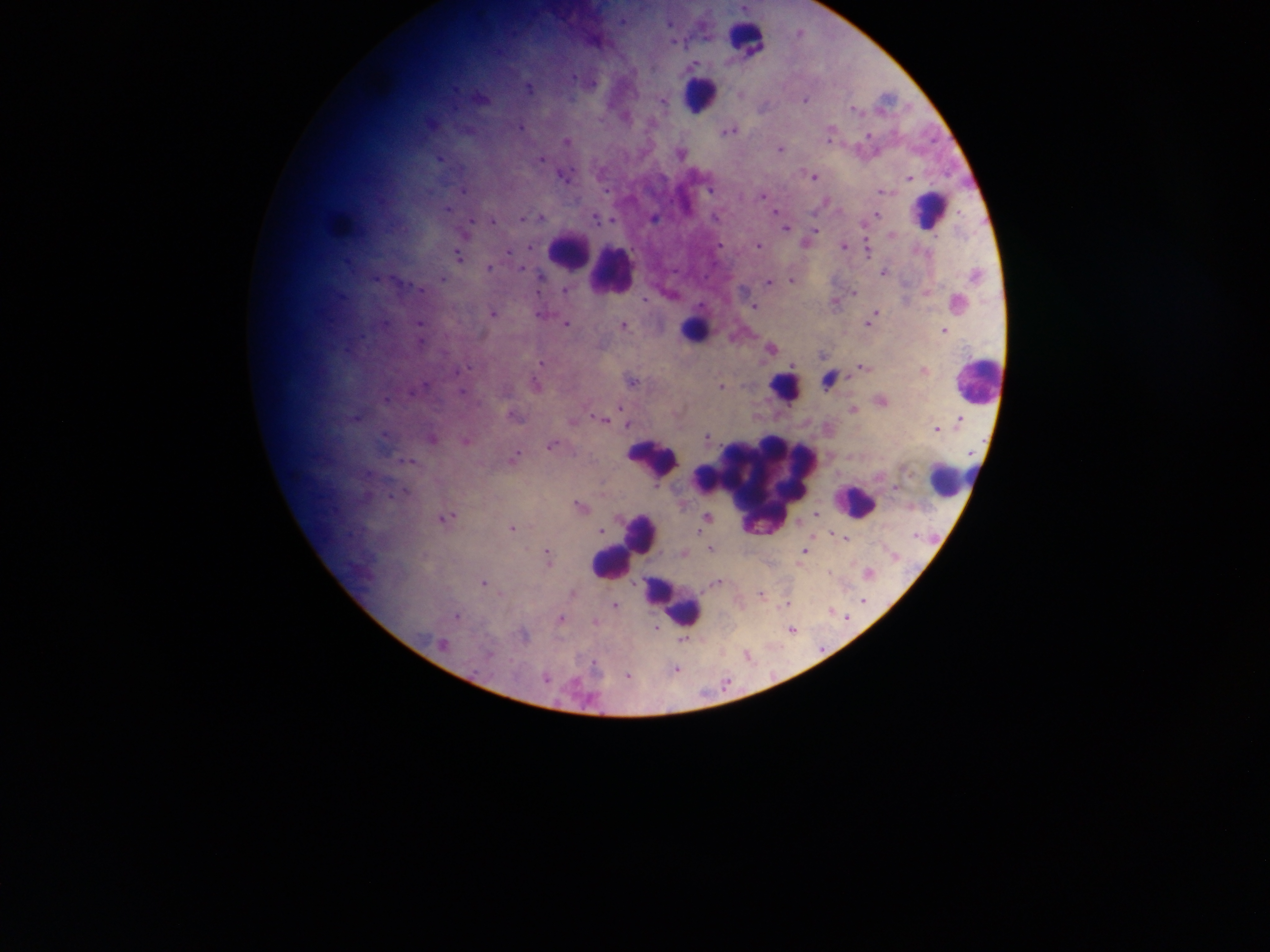
Approximate centers as x y in pixels.
Summary:
  - Leukocyte locations: 746 44; 697 97; 925 210; 342 224; 564 248; 605 270; 696 320; 972 382; 780 384; 646 453; 953 487; 760 488; 853 504; 647 533; 610 563; 679 602
  - Plasmodium parasite locations: 576 78; 531 90; 743 96; 806 102; 854 110; 857 113; 520 128; 733 132; 729 134; 829 135; 870 137; 567 142; 782 151; 680 154; 815 178; 909 180; 710 190; 880 193; 767 194; 764 197; 774 211; 879 216; 523 219; 543 219; 718 219; 597 221; 494 223; 786 229; 817 230; 815 234; 720 245; 534 246; 758 248; 845 249; 511 250; 870 254; 459 258; 520 266; 489 267; 886 272; 443 279; 769 282; 791 282; 539 290; 420 291; 567 291; 854 294; 645 300; 753 307; 877 313; 537 314; 493 315; 872 319; 387 324; 567 324; 868 325; 419 326; 624 326; 483 335; 420 346; 771 350; 543 362; 862 369; 632 381; 535 388; 427 389; 721 389; 464 394; 622 407; 853 411; 593 415; 359 420; 608 420; 962 421; 629 425; 937 432; 384 436; 708 438; 434 440; 467 442; 551 447; 970 456; 516 457; 411 463; 301 479; 406 495; 394 496; 580 507; 454 516; 816 516; 707 518; 444 520; 512 530; 600 532; 700 532; 833 535; 918 536; 845 539; 806 548; 709 550; 804 551; 685 553; 548 554; 896 560; 549 564; 867 575; 484 583; 490 587; 571 595; 761 596; 864 600; 616 607; 830 612; 457 616; 847 617; 561 620; 597 622; 656 628; 792 631; 524 638; 684 641; 442 646; 750 659; 547 679; 726 685
  - Field of view: single
  - Capture: mobile-phone photograph through a microscope
  - Country: Ghana
  - Preparation: thick blood smear
  - Image size: 1270×952 pixels